Name the cell type shown.
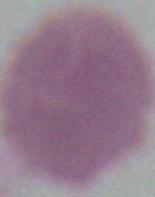

This is an erythrocyte.

magnification: 1000x
modality: micrograph